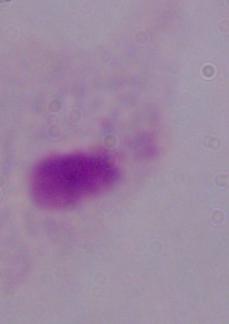

magnification = 1000x
identification = trichomonad
modality = photomicrograph